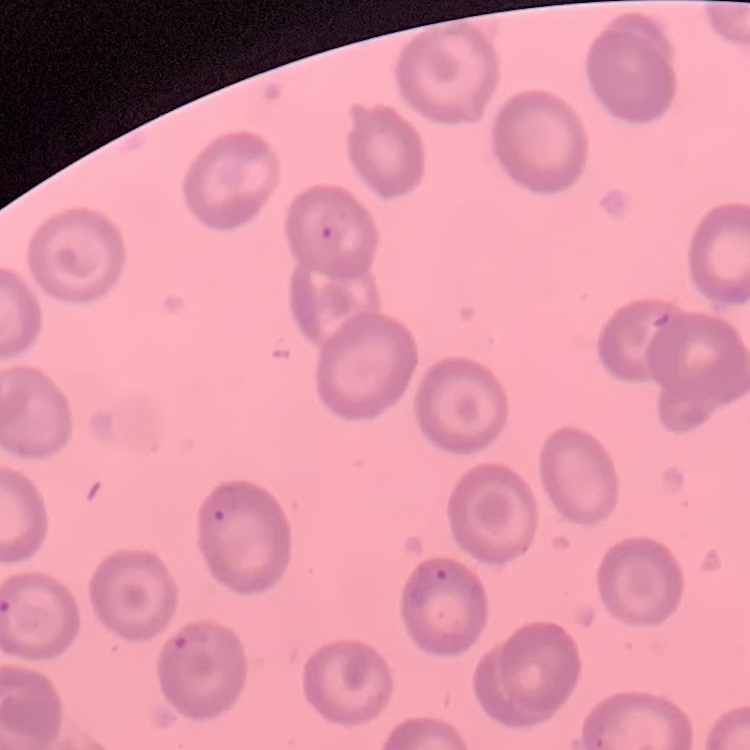

erythrocyte_morphology: no rouleaux formation
stain: Field's or Giemsa
preparation: thin blood film
image_type: square crop of a larger photomicrograph